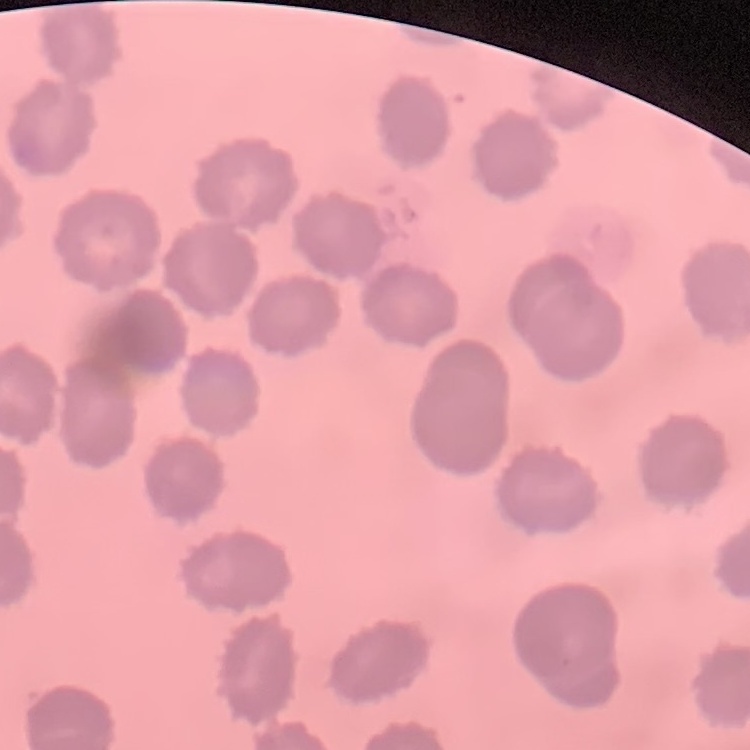

The erythrocytes exhibit no rouleaux formation. Field's or Giemsa stain. One tile cut from a larger photomicrograph. Thin peripheral smear.